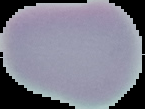

Segmented cell region on a black background. From a thin blood film. Image is 145×109 pixels. Malaria status: uninfected.